Locate every leukocyte (white blood cell).
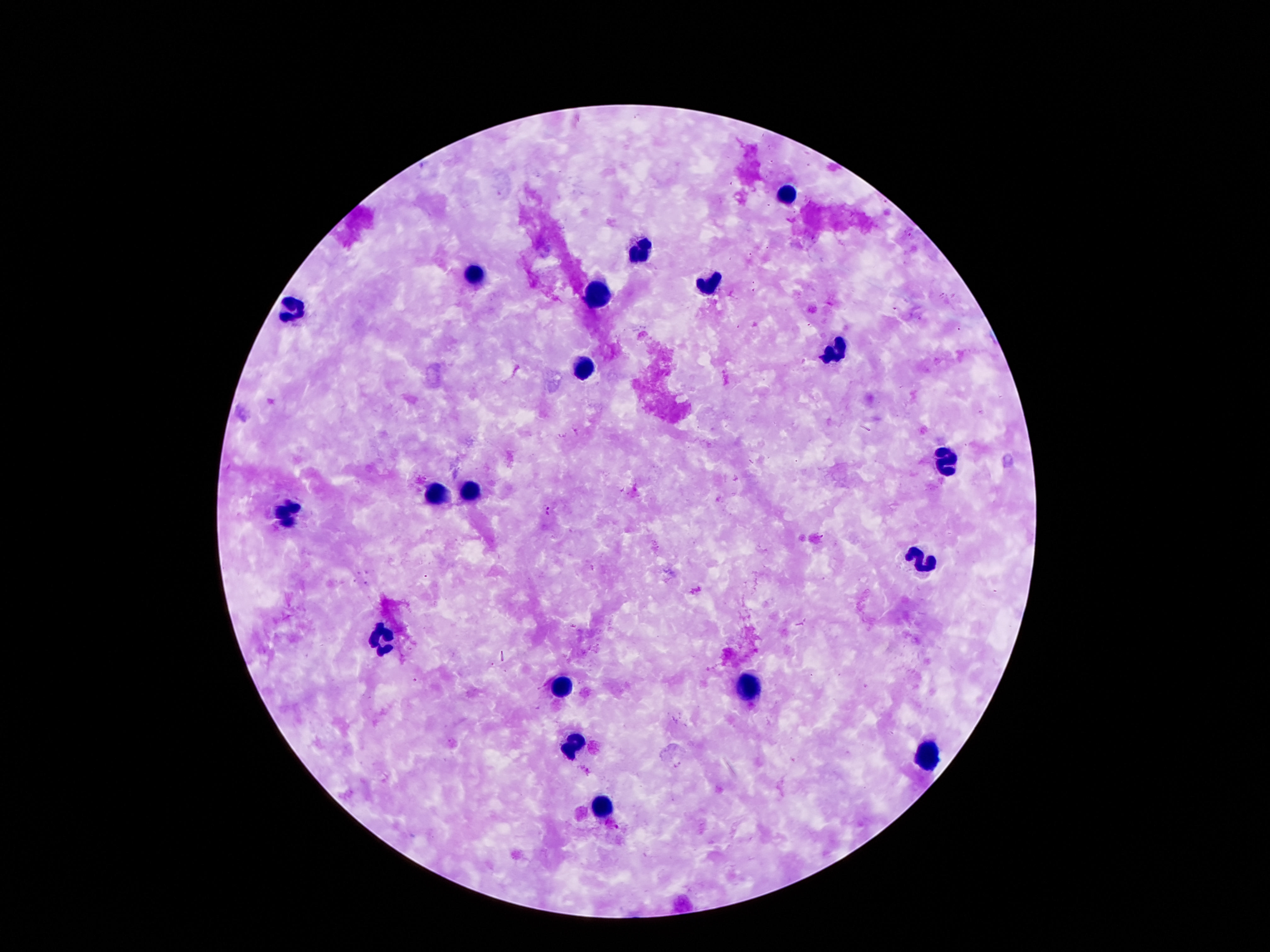

Approximate object centers, in pixels from the top-left corner.
Leukocytes: (x=789, y=195), (x=642, y=252), (x=475, y=277), (x=713, y=286), (x=599, y=294), (x=292, y=308), (x=834, y=348), (x=584, y=365), (x=944, y=464), (x=470, y=492), (x=434, y=498), (x=291, y=514), (x=922, y=561), (x=380, y=640), (x=563, y=688), (x=752, y=688), (x=576, y=744), (x=925, y=756), (x=606, y=810).

capture = smartphone camera through the microscope eyepiece
stain = Giemsa
patient malaria status = negative
field of view = single
image size = 1270×952 pixels
magnification = 100x
preparation = thick peripheral-blood smear